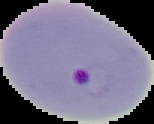
preparation: thin blood smear
image_type: segmented cell region with the area outside set to black
result: Plasmodium parasites identified
image_size: 154×124 pixels